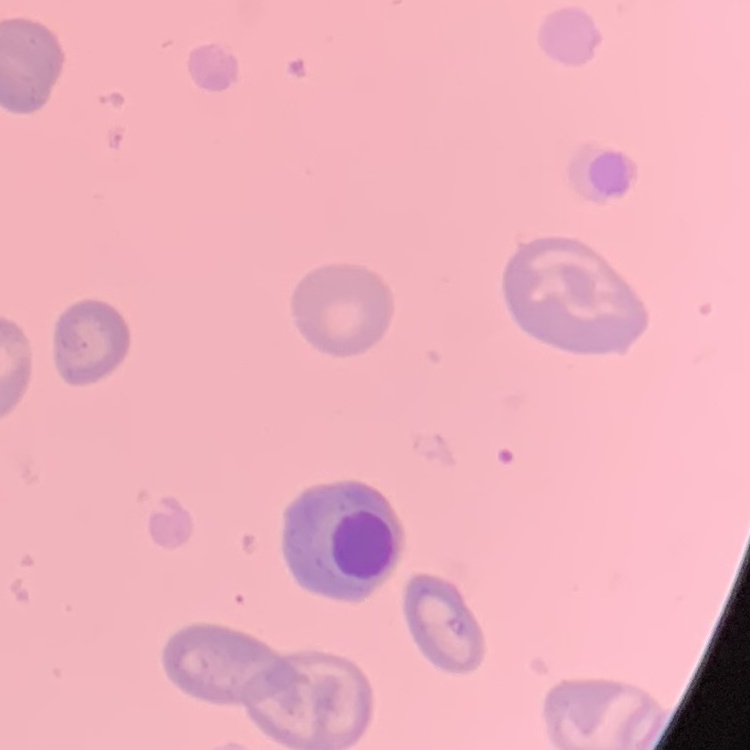

Summary:
  - Red blood cell morphology: no rouleaux formation
  - Preparation: thin blood film
  - Image type: square crop of a larger photomicrograph
  - Stain: Field's or Giemsa